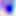

modality = micrograph
magnification = 400x
identification = Toxoplasma gondii